Locate every malaria parasite.
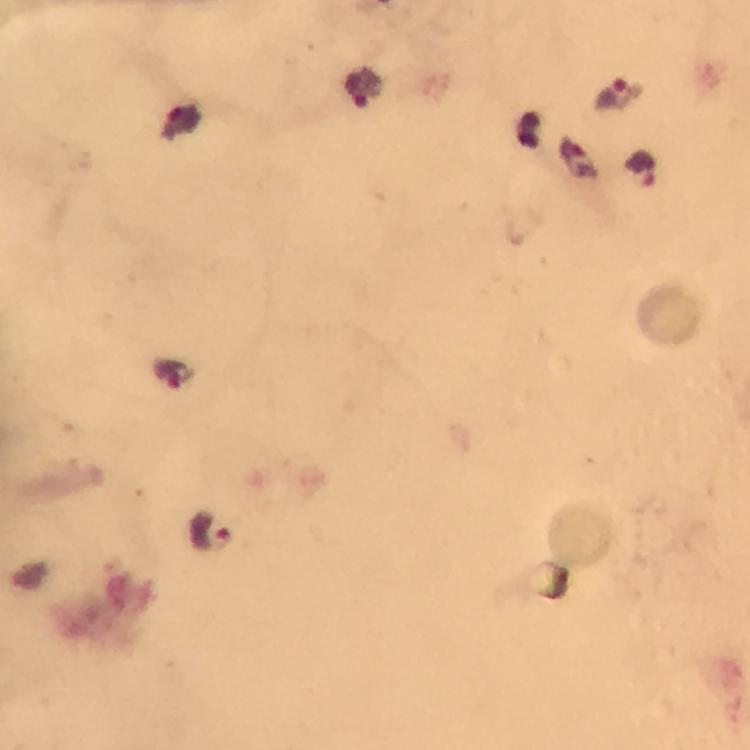
Approximate centers as [x, y] in pixels.
Malaria parasites: [363, 90], [617, 94], [576, 157], [641, 169], [171, 376], [210, 532].

capture: smartphone camera through the microscope
immersion_oil: used
stain: Giemsa
magnification: 100x
image_size: 750×750 pixels
preparation: thick smear
cropped_from: a single field of view
context: from a malaria diagnostic workup